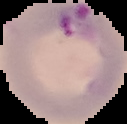
Segmented cell region on a black background. Malaria status: parasitized. Image is 127×124 pixels. From a thin blood film.